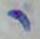 Micrograph. Toxoplasma gondii is shown. 1000x magnification.